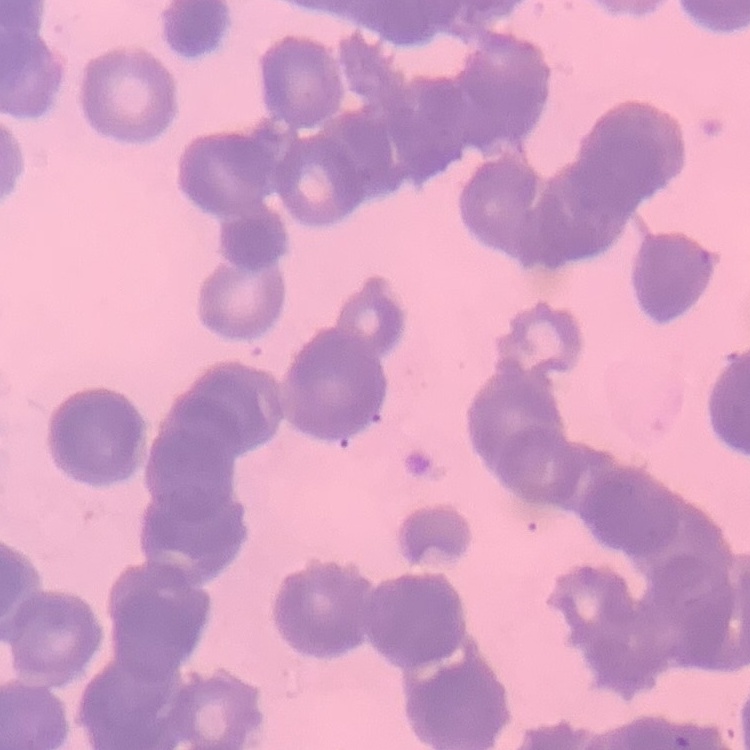

red blood cell morphology = rouleaux formation
preparation = thin blood smear
stain = Field's or Giemsa
image type = square crop of a larger photomicrograph